Identify the cell.
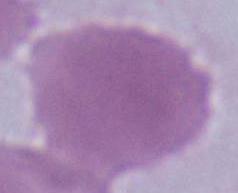
This is an erythrocyte.

Summary:
  - Modality: micrograph
  - Magnification: 1000x